Comment on the morphology of the red blood cells.
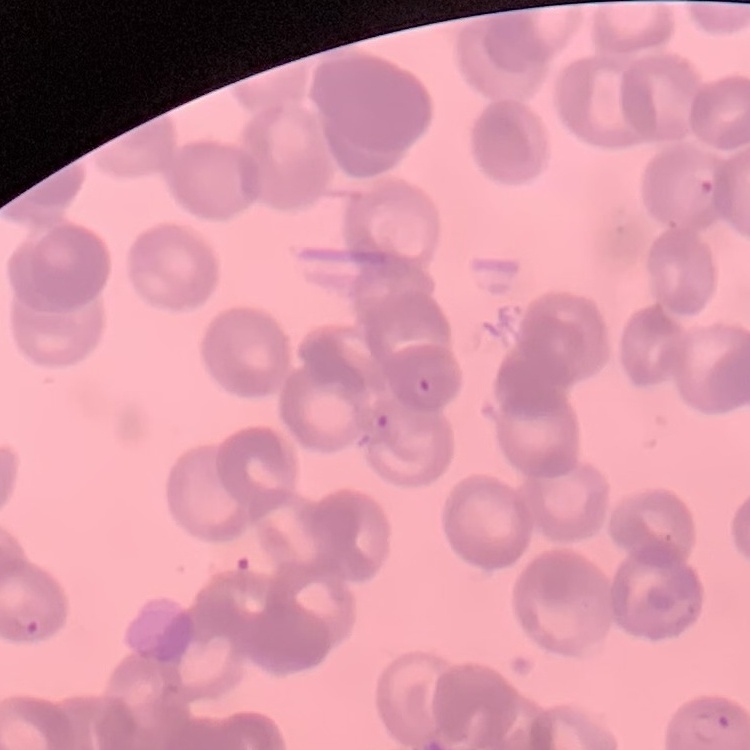
They show rouleaux formation.

{
  "preparation": "thin blood film",
  "stain": "Field's or Giemsa",
  "image_type": "square crop of a larger photomicrograph"
}